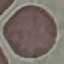

malaria status = uninfected
preparation = thin smear
image type = automatically extracted cell patch, resized to 64 × 64 pixels
capture = smartphone through the microscope eyepiece
stain = Giemsa